Identify the preparation type.
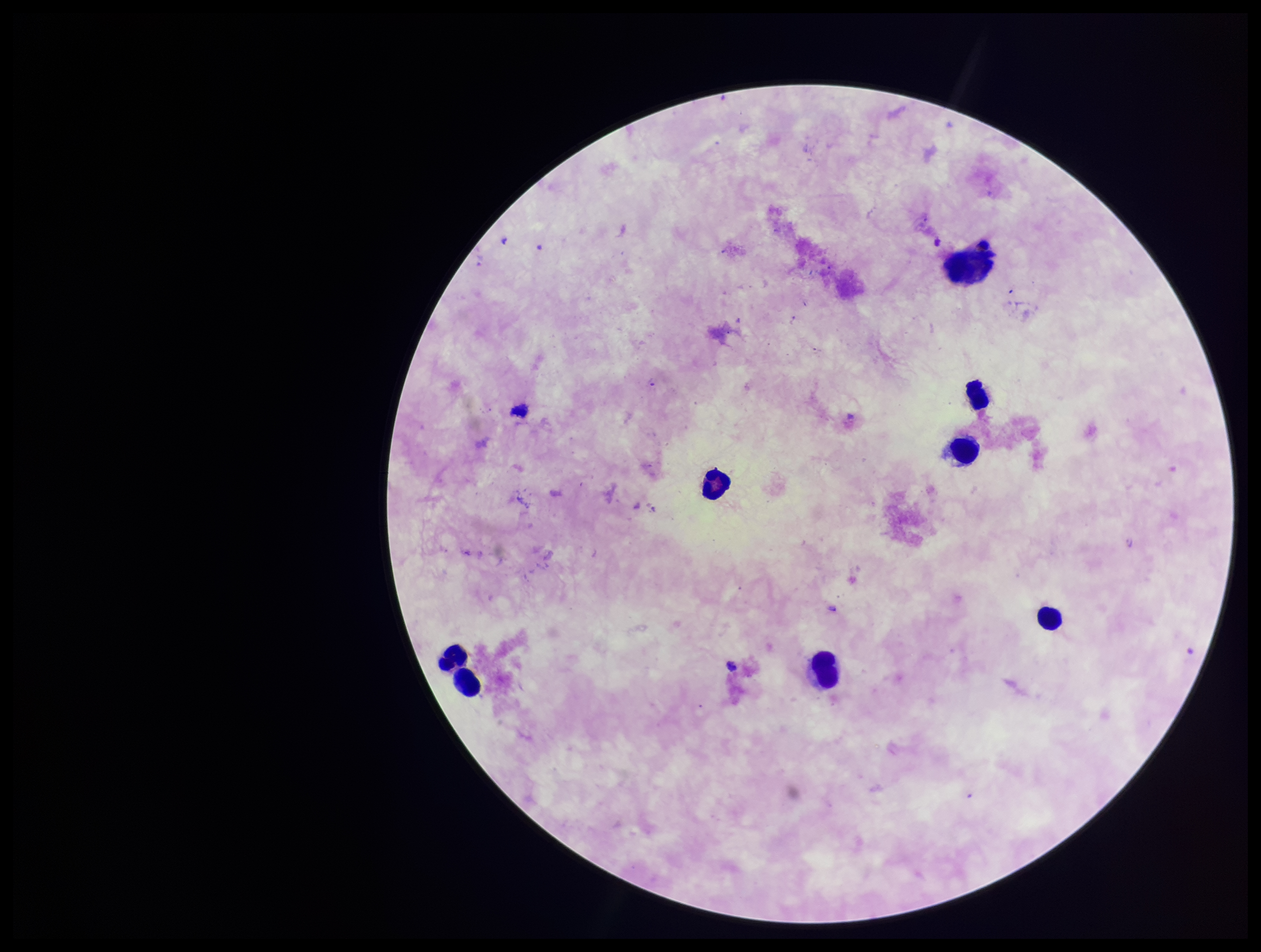

It is a thick blood smear.

Leukocyte count: 7. Stained with Giemsa. Single field of view. Patient malaria status: negative. Smartphone photograph taken through the eyepiece of a microscope. Plasmodium parasites: none seen. Parasite count: 0. Image is 1261×952 pixels.